Locate every blood parasite and identify its species.
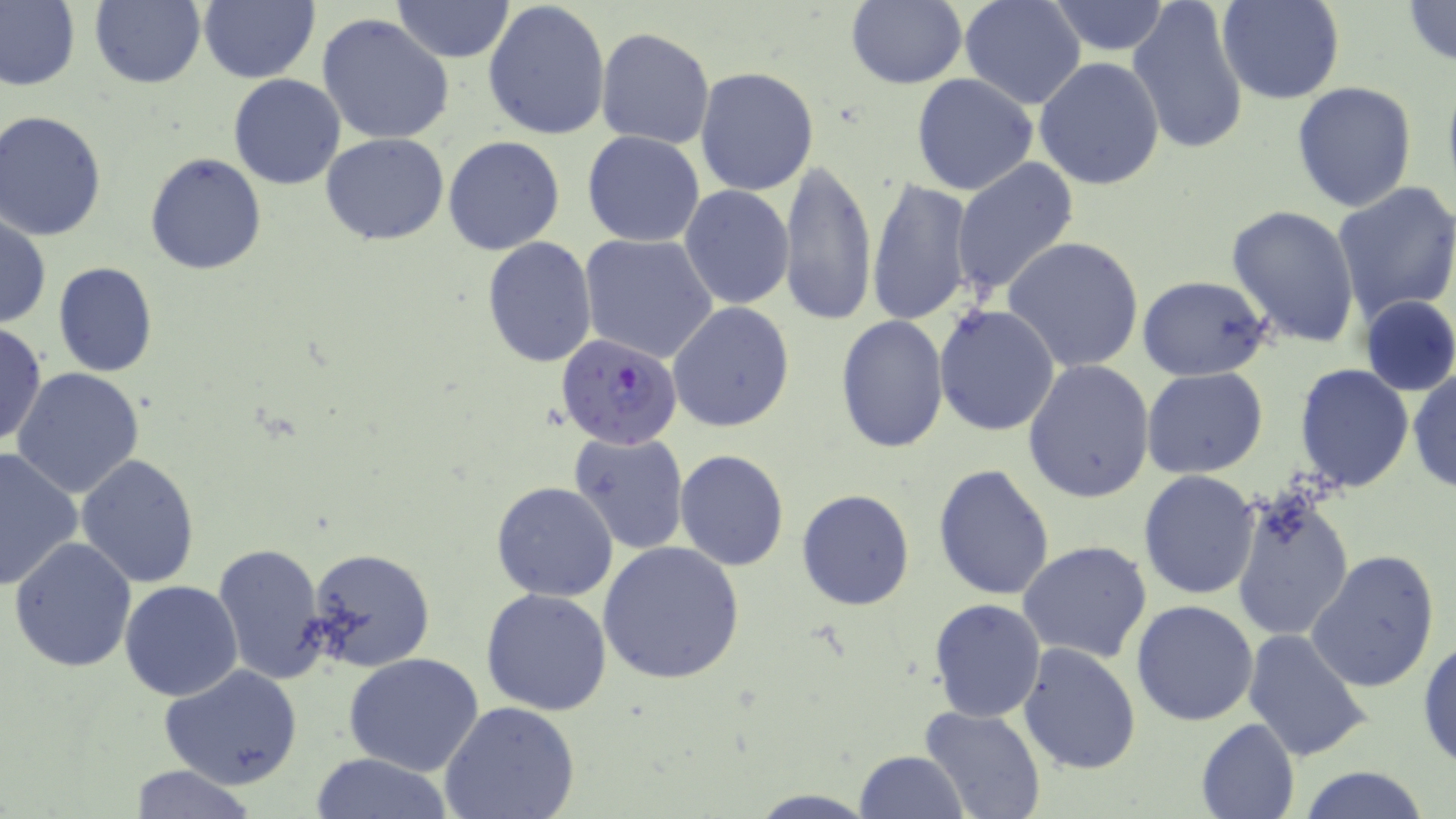
Approximate bounding boxes as (x1, y1, x2, y2) in pixels.
Plasmodium falciparum-infected red blood cells: (556, 333, 683, 449).
No Plasmodium ovale, Plasmodium malariae, Plasmodium vivax, Babesia divergens, or Trypanosoma brucei observed.

Uninfected red blood cell locations: (0, 0, 80, 92), (91, 0, 206, 88), (389, 0, 515, 63), (482, 0, 611, 142), (960, 0, 1086, 109), (1128, 0, 1249, 158), (1218, 0, 1346, 105), (1402, 0, 1456, 68), (198, 1, 319, 83), (845, 1, 967, 90), (1044, 1, 1173, 55), (317, 15, 454, 146), (596, 26, 714, 150), (1034, 56, 1167, 192), (694, 67, 819, 196), (1441, 70, 1456, 203), (911, 73, 1039, 194), (228, 74, 345, 190), (1291, 81, 1417, 211), (0, 110, 108, 241), (581, 131, 706, 247), (320, 133, 449, 245), (444, 136, 565, 256), (144, 153, 267, 275), (951, 157, 1079, 301), (777, 159, 877, 327), (865, 178, 975, 329), (1331, 181, 1456, 325), (679, 185, 795, 310), (1227, 204, 1360, 347), (0, 213, 49, 329), (579, 232, 720, 364), (1002, 235, 1144, 373), (481, 236, 598, 370), (53, 261, 158, 378), (41, 262, 153, 492), (1137, 275, 1274, 382), (1357, 295, 1456, 397), (667, 302, 795, 434), (933, 304, 1061, 436), (834, 315, 949, 453), (0, 323, 47, 446), (1022, 360, 1155, 504), (1295, 363, 1414, 492), (1142, 367, 1268, 479), (1407, 367, 1455, 493), (11, 368, 146, 499), (569, 431, 690, 555), (0, 446, 85, 589), (675, 448, 789, 570), (76, 454, 200, 590), (932, 464, 1056, 599), (1138, 470, 1260, 599), (491, 481, 619, 601), (1229, 487, 1355, 645), (795, 488, 917, 611), (9, 536, 138, 671), (1018, 539, 1153, 665), (212, 540, 329, 684), (597, 541, 746, 685), (307, 547, 436, 674), (1306, 549, 1441, 694), (119, 580, 243, 702), (481, 588, 613, 715), (929, 598, 1046, 722), (1131, 598, 1260, 726), (1242, 629, 1372, 765), (1417, 636, 1456, 772), (1017, 641, 1143, 776), (344, 653, 483, 775), (160, 666, 304, 789), (439, 701, 582, 819), (921, 706, 1045, 819), (1196, 718, 1301, 819), (854, 750, 969, 818), (312, 752, 454, 818), (127, 764, 258, 819), (1297, 765, 1432, 819), (746, 790, 879, 818). Slide-level diagnosis: Plasmodium falciparum. Image is 1456×819 pixels. Single field of view. May-Grünwald-Giemsa stain. Light microscopy. Thin blood film. 1000x magnification.